Point out each Plasmodium parasite and each leukocyte.
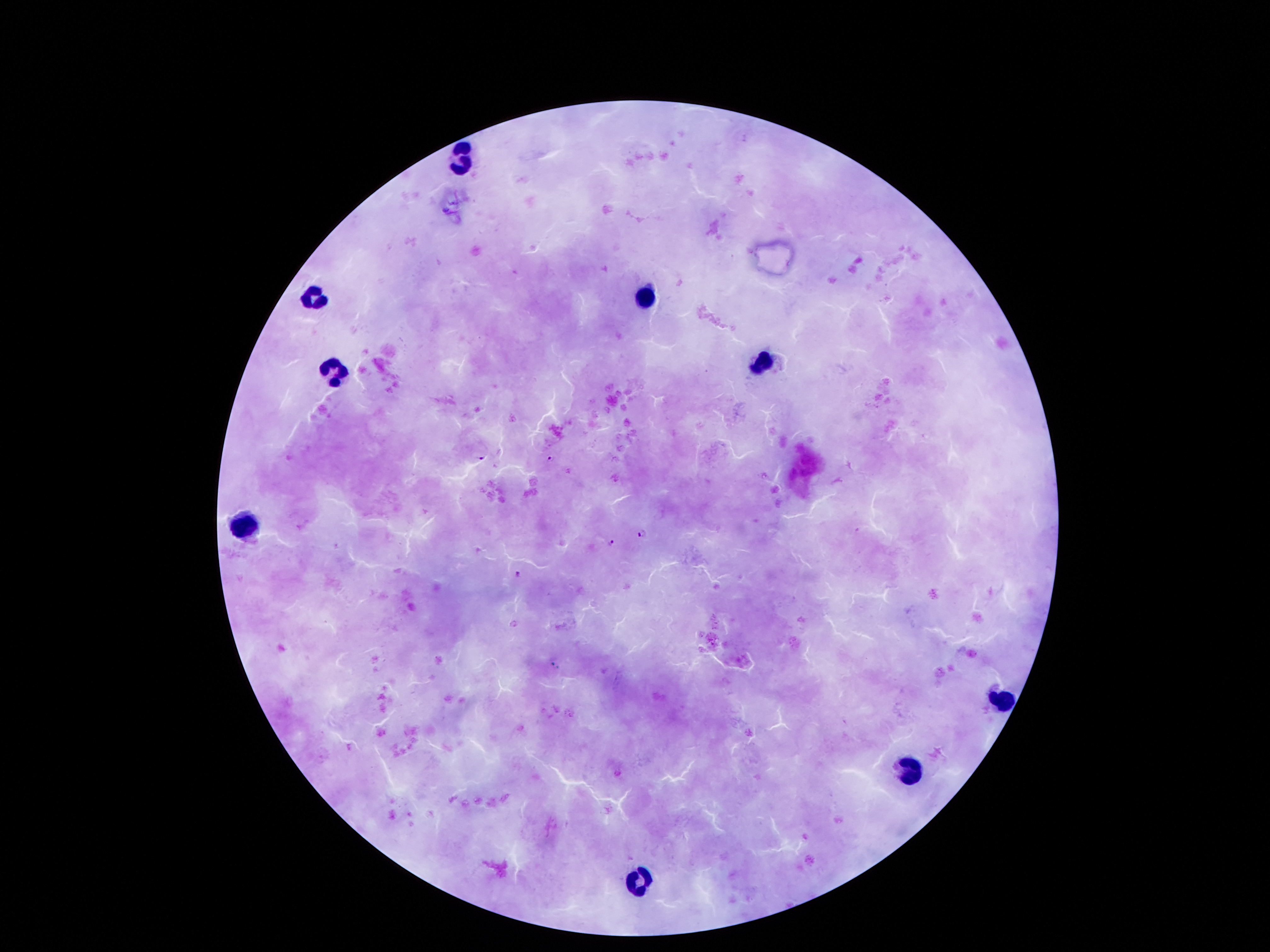

Approximate centers as [x, y] in pixels.
Plasmodium parasites: [481, 456], [553, 459], [642, 533], [612, 542], [516, 575].
Leukocytes: [463, 163], [644, 299], [315, 301], [761, 360], [335, 376], [242, 528], [996, 702], [912, 770], [637, 877].

Giemsa-stained preparation. One field from this slide. Image is 1270×952 pixels. Patient malaria status: positive for Plasmodium falciparum. Thick blood film. 100x magnification. Photographed through the microscope eyepiece with a smartphone camera.